Assess the morphology of the erythrocytes.
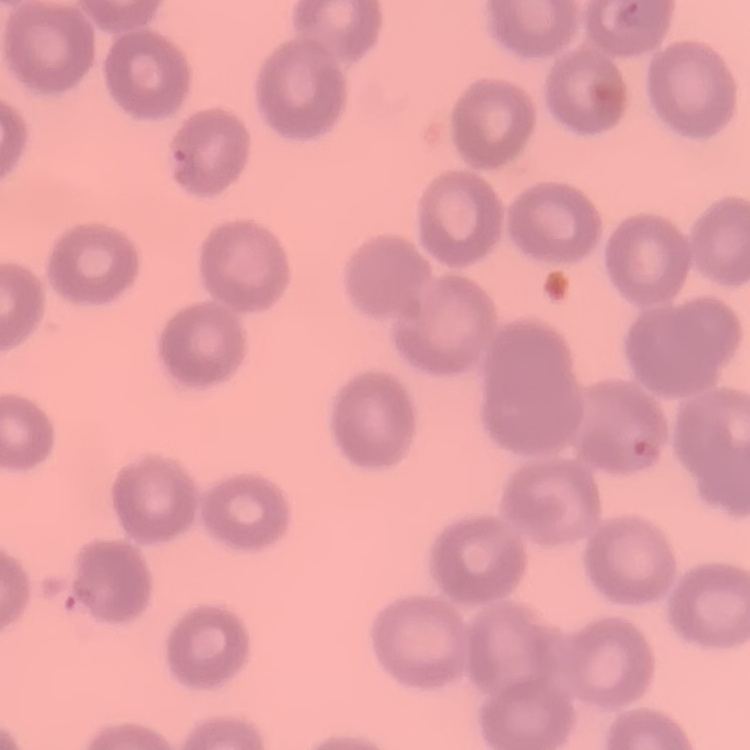
They show no rouleaux formation.

preparation = thin peripheral smear
stain = Field's or Giemsa
image type = square crop of a larger photomicrograph